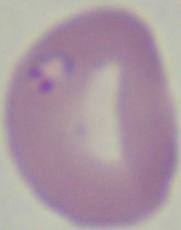
Summary:
  - Modality: micrograph
  - Magnification: 1000x
  - Identification: Babesia